Report the malaria status.
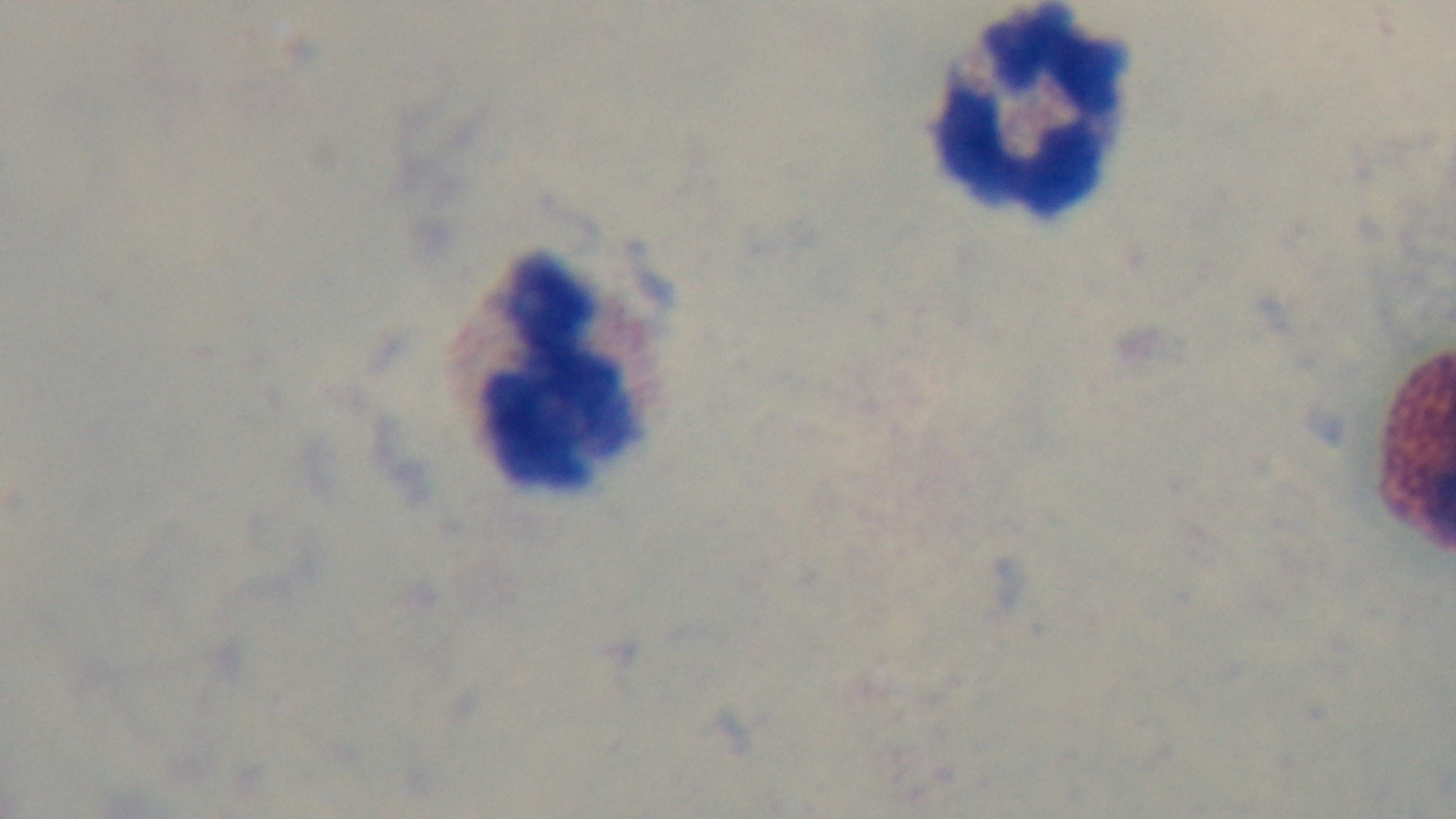

Negative.

100x oil-immersion objective. Light microscopy. Preparation: thick smear. Single field of view. Captured with a mounted 4K digital camera. Giemsa-stained.